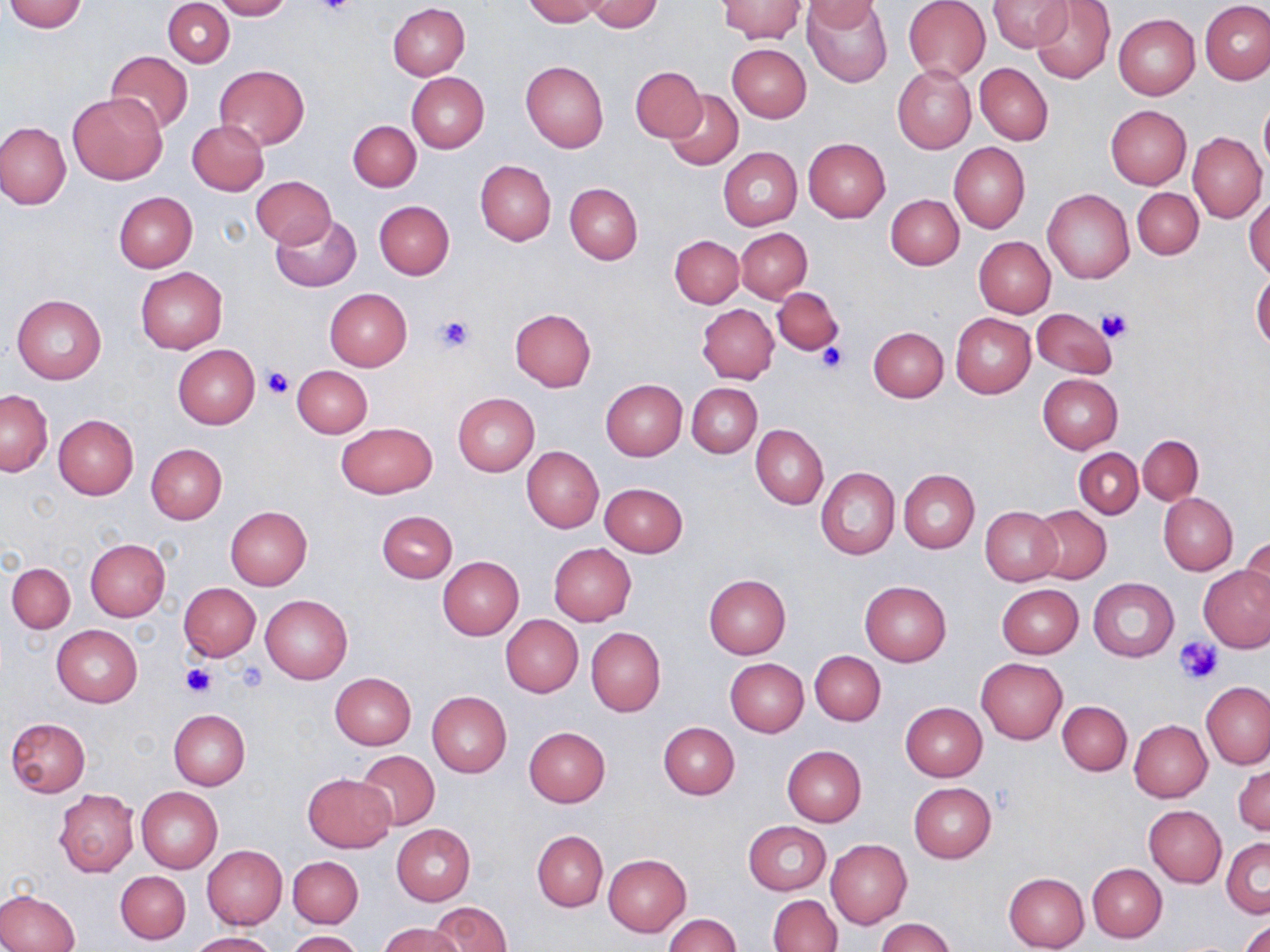
Summary:
  - Coordinate format: approximate bounding boxes as [x1, y1, x2, y2] in pixels
  - Platelet locations: [316, 0, 358, 19], [1095, 305, 1134, 343], [437, 315, 473, 352], [816, 343, 847, 374], [264, 367, 292, 398], [1177, 636, 1224, 683], [235, 662, 268, 693], [181, 663, 213, 697]
  - Uninfected red blood cell locations: [4, 0, 88, 32], [164, 0, 234, 68], [214, 0, 290, 20], [522, 0, 607, 25], [717, 0, 806, 43], [803, 0, 893, 87], [903, 0, 991, 83], [989, 0, 1074, 53], [1030, 0, 1115, 83], [585, 1, 664, 33], [801, 1, 886, 31], [1200, 1, 1270, 85], [388, 4, 470, 80], [1113, 14, 1199, 99], [727, 44, 811, 123], [105, 50, 193, 134], [521, 60, 609, 153], [975, 63, 1053, 145], [214, 65, 309, 150], [631, 65, 706, 141], [892, 65, 977, 154], [407, 72, 489, 153], [665, 89, 743, 170], [69, 92, 168, 185], [1258, 102, 1270, 174], [1105, 105, 1191, 189], [188, 120, 268, 195], [348, 120, 421, 190], [0, 121, 71, 208], [1187, 131, 1267, 224], [804, 137, 890, 222], [950, 143, 1029, 232], [718, 146, 802, 230], [475, 160, 556, 245], [250, 175, 337, 248], [564, 182, 643, 264], [1132, 187, 1204, 260], [1043, 189, 1134, 284], [114, 192, 197, 273], [885, 194, 963, 269], [1245, 195, 1270, 280], [374, 201, 454, 279], [270, 212, 362, 292], [736, 228, 812, 303], [670, 235, 744, 309], [973, 236, 1055, 318], [135, 267, 228, 354], [1252, 272, 1270, 351], [772, 287, 844, 356], [325, 288, 412, 371], [12, 294, 107, 384], [697, 304, 779, 384], [510, 308, 597, 390], [1032, 309, 1119, 377], [950, 313, 1036, 397], [869, 326, 949, 402], [173, 345, 260, 428], [291, 366, 372, 438], [1037, 373, 1124, 452], [600, 378, 687, 460], [687, 382, 762, 458], [1, 391, 52, 476], [453, 393, 538, 475], [53, 415, 138, 499], [336, 422, 437, 499], [751, 425, 827, 508], [1137, 434, 1204, 505], [147, 443, 227, 523], [521, 446, 603, 533], [1074, 448, 1143, 518], [815, 466, 899, 560], [899, 469, 980, 552], [600, 483, 688, 557], [1159, 493, 1238, 575], [1030, 505, 1111, 584], [225, 506, 312, 590], [980, 506, 1062, 585], [377, 510, 457, 582], [1240, 537, 1270, 612], [84, 538, 171, 622], [549, 543, 636, 626], [437, 556, 524, 640], [7, 562, 75, 634], [1200, 565, 1270, 652], [704, 574, 791, 658], [1088, 577, 1178, 662], [860, 581, 952, 667], [179, 583, 260, 661], [996, 585, 1083, 659], [261, 594, 352, 683], [500, 615, 584, 697], [52, 624, 142, 706], [585, 627, 666, 716], [810, 651, 886, 725], [725, 658, 808, 736], [975, 658, 1066, 744], [330, 672, 416, 749], [1201, 682, 1269, 769], [427, 691, 512, 776], [1057, 700, 1131, 775], [901, 702, 987, 781], [169, 710, 249, 790], [6, 718, 90, 797], [1129, 719, 1212, 802], [658, 721, 740, 799], [524, 726, 611, 806], [781, 746, 867, 826], [356, 750, 440, 829], [1234, 764, 1269, 837], [303, 773, 396, 852], [909, 783, 997, 862], [135, 786, 222, 874], [54, 789, 139, 877], [1144, 805, 1226, 887], [743, 821, 831, 896], [391, 823, 475, 905], [532, 830, 608, 911], [1222, 838, 1269, 917], [826, 839, 910, 928], [201, 844, 286, 929], [603, 853, 691, 936], [288, 855, 363, 928], [1088, 863, 1167, 942], [116, 872, 191, 944], [1004, 872, 1090, 952], [0, 889, 79, 952], [769, 894, 841, 952], [431, 902, 512, 952], [662, 913, 741, 952], [876, 918, 956, 952], [1239, 919, 1270, 952], [379, 923, 460, 952], [285, 930, 362, 952], [186, 932, 276, 952]
  - Slide-level diagnosis: no evidence of blood parasites
  - Image size: 1270×952 pixels
  - Preparation: thin blood smear
  - Modality: light microscopy
  - Magnification: 1000x
  - Field of view: one of a larger specimen
  - Stain: May-Grünwald-Giemsa